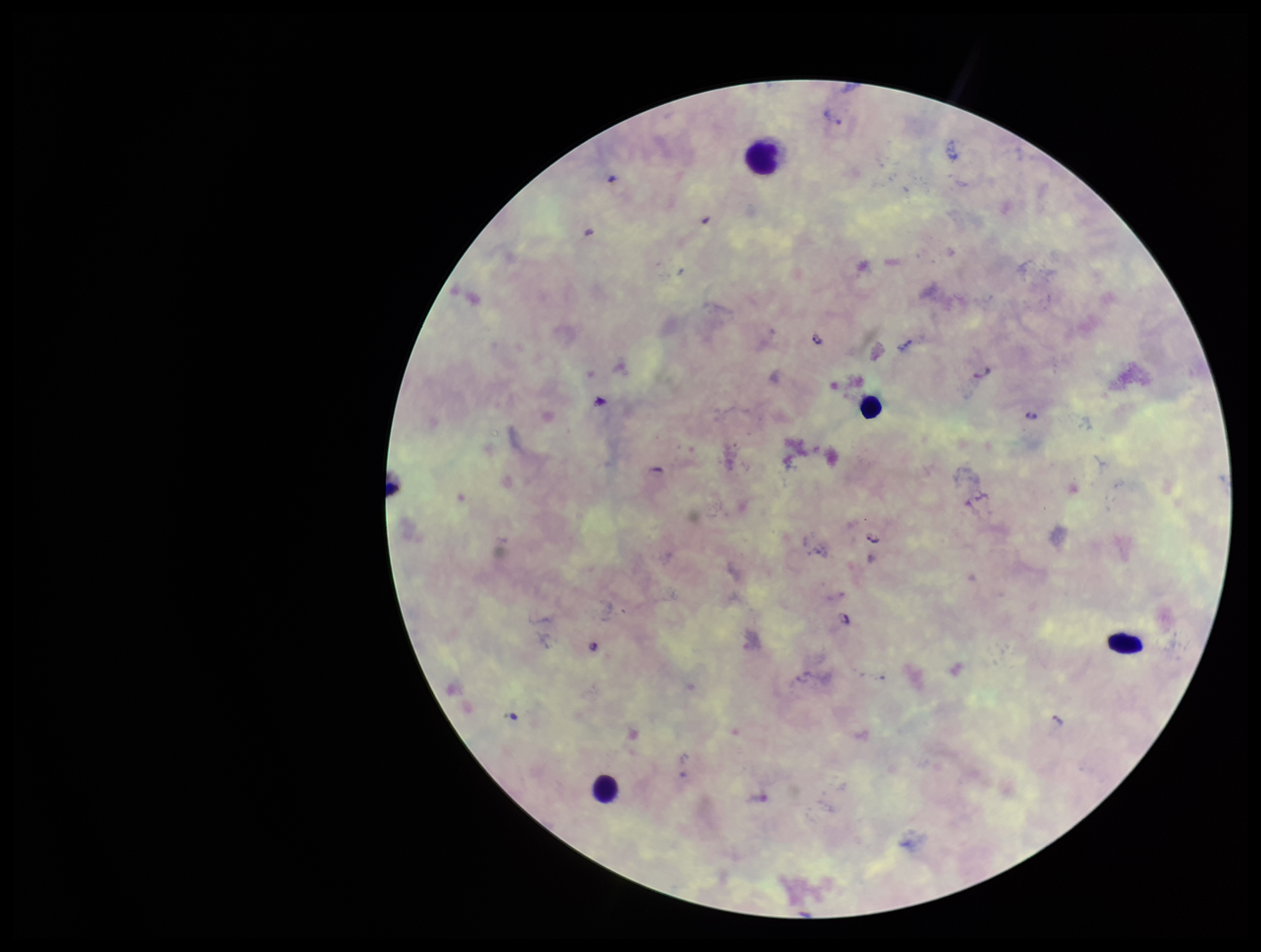

Summary:
  - Patient malaria status: positive
  - Stain: Giemsa
  - Species reported for this patient: Plasmodium falciparum
  - Capture: smartphone photograph through the microscope eyepiece
  - Preparation: thick blood smear
  - Field of view: one from this slide
  - Image size: 1261×952 pixels
  - Plasmodium parasites: detected
  - Leukocyte count: 4
  - Parasite count: 5